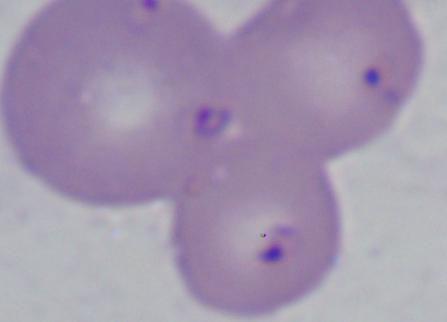

Summary:
  - Modality: photomicrograph
  - Magnification: 1000x
  - Identification: Babesia